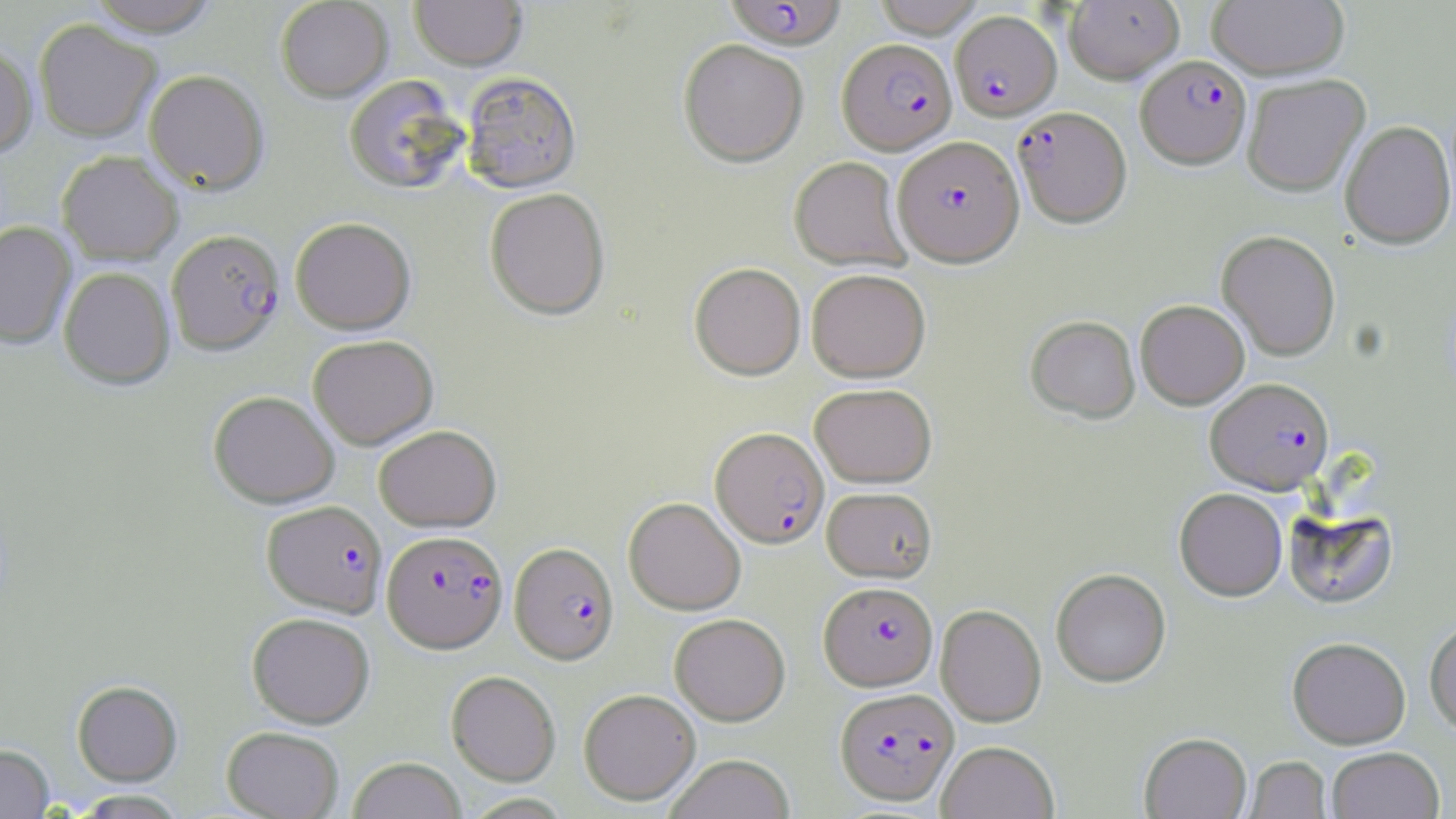 Approximate bounding boxes as named x1/y1/x2/y2 corners in pixels. Plasmodium falciparum-infected red blood cell locations: (x1=724, y1=0, x2=846, y2=50), (x1=950, y1=10, x2=1061, y2=121), (x1=837, y1=38, x2=957, y2=155), (x1=1136, y1=55, x2=1251, y2=168), (x1=1013, y1=106, x2=1131, y2=228), (x1=892, y1=135, x2=1024, y2=266), (x1=167, y1=228, x2=284, y2=356), (x1=1205, y1=377, x2=1334, y2=494), (x1=711, y1=426, x2=829, y2=548), (x1=261, y1=500, x2=387, y2=617), (x1=383, y1=530, x2=508, y2=653), (x1=510, y1=542, x2=619, y2=665), (x1=819, y1=581, x2=937, y2=690), (x1=835, y1=687, x2=959, y2=806). Uninfected red blood cell locations: (x1=86, y1=0, x2=220, y2=37), (x1=275, y1=0, x2=392, y2=102), (x1=410, y1=0, x2=526, y2=72), (x1=872, y1=0, x2=985, y2=37), (x1=1064, y1=0, x2=1184, y2=84), (x1=1208, y1=1, x2=1349, y2=79), (x1=34, y1=20, x2=161, y2=142), (x1=678, y1=39, x2=808, y2=168), (x1=0, y1=41, x2=37, y2=159), (x1=144, y1=69, x2=269, y2=194), (x1=461, y1=73, x2=581, y2=194), (x1=1242, y1=74, x2=1370, y2=196), (x1=343, y1=75, x2=467, y2=194), (x1=1340, y1=120, x2=1455, y2=249), (x1=57, y1=150, x2=183, y2=265), (x1=789, y1=157, x2=911, y2=271), (x1=485, y1=187, x2=610, y2=320), (x1=290, y1=217, x2=416, y2=334), (x1=0, y1=221, x2=76, y2=349), (x1=1216, y1=230, x2=1341, y2=360), (x1=689, y1=262, x2=806, y2=380), (x1=59, y1=267, x2=174, y2=390), (x1=806, y1=268, x2=931, y2=382), (x1=1135, y1=300, x2=1249, y2=409), (x1=1025, y1=315, x2=1140, y2=423), (x1=308, y1=334, x2=438, y2=449), (x1=809, y1=383, x2=937, y2=487), (x1=208, y1=390, x2=339, y2=508), (x1=374, y1=424, x2=501, y2=532), (x1=822, y1=486, x2=937, y2=582), (x1=1174, y1=488, x2=1287, y2=601), (x1=623, y1=497, x2=745, y2=615), (x1=1284, y1=505, x2=1398, y2=611), (x1=1051, y1=568, x2=1171, y2=687), (x1=935, y1=604, x2=1046, y2=727), (x1=247, y1=612, x2=375, y2=728), (x1=669, y1=613, x2=790, y2=725), (x1=1424, y1=618, x2=1456, y2=736), (x1=1288, y1=636, x2=1411, y2=748), (x1=446, y1=671, x2=561, y2=785), (x1=72, y1=680, x2=182, y2=785), (x1=579, y1=688, x2=701, y2=805), (x1=221, y1=726, x2=344, y2=819), (x1=1140, y1=732, x2=1251, y2=819), (x1=937, y1=740, x2=1059, y2=819), (x1=0, y1=744, x2=54, y2=818), (x1=1326, y1=746, x2=1445, y2=819), (x1=664, y1=754, x2=795, y2=819), (x1=1244, y1=756, x2=1332, y2=818), (x1=348, y1=757, x2=466, y2=819), (x1=71, y1=789, x2=187, y2=818). Slide-level diagnosis: Plasmodium falciparum. Thin blood film. Image is 1456×819 pixels. Single field of view. Captured at 1000x magnification. Optical microscopy. May-Grünwald-Giemsa-stained preparation.